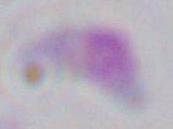

magnification = 1000x
modality = micrograph
identification = Toxoplasma gondii